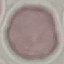 Result: no malaria parasites detected. Giemsa-stained preparation. Acquired by smartphone through the microscope eyepiece. Automatically extracted cell patch, resized to 64 × 64 pixels. Thin smear of blood.